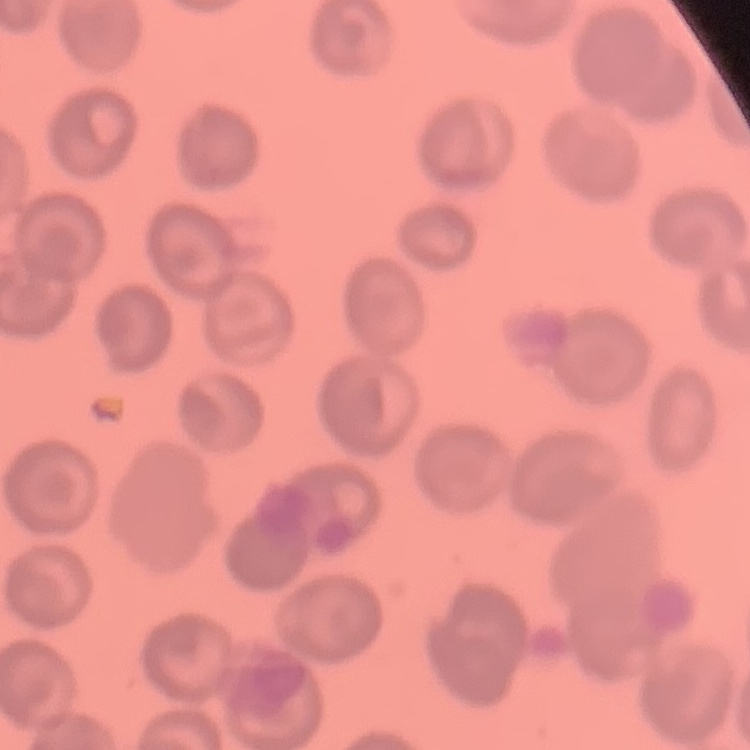
erythrocyte morphology = no rouleaux formation
stain = Field's or Giemsa
image type = one tile cut from a larger photomicrograph
preparation = thin blood smear